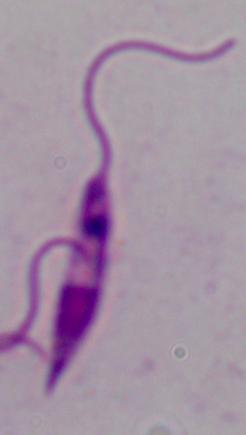
{
  "modality": "photomicrograph",
  "magnification": "1000x",
  "identification": "Leishmania"
}